Locate and identify every blood parasite.
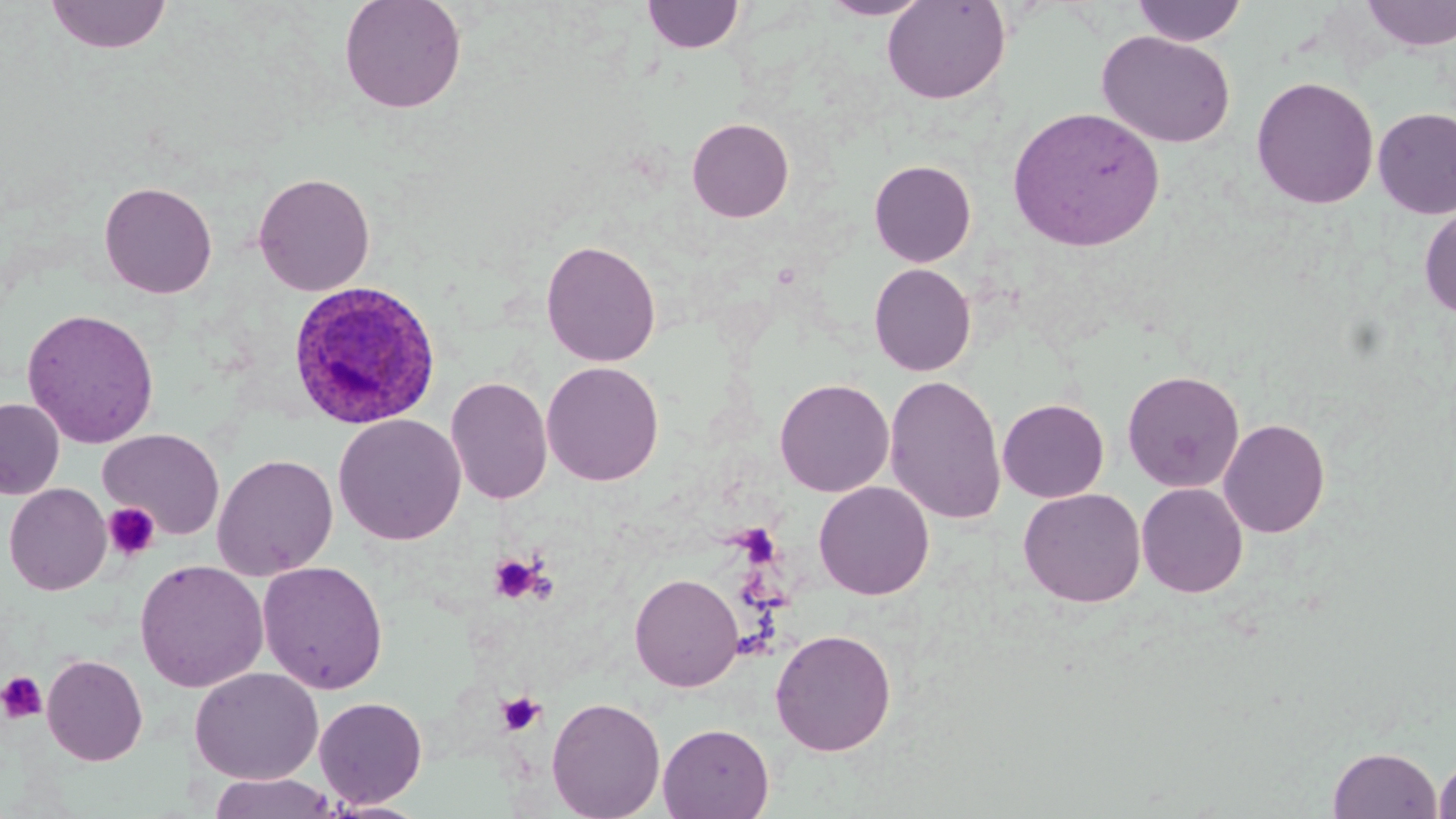
Approximate bounding boxes as (x1,y1)-(x2,y2) corner pairs in pixels.
Plasmodium ovale-infected red blood cells: (287,281)-(442,430).
No Plasmodium falciparum, Plasmodium malariae, Plasmodium vivax, Babesia divergens, or Trypanosoma brucei observed.

Platelet locations: (102,502)-(160,561), (488,552)-(545,604), (0,672)-(48,724), (497,690)-(545,736). Uninfected red blood cell locations: (45,0)-(172,55), (339,0)-(467,114), (818,0)-(934,20), (882,0)-(1010,104), (1360,0)-(1456,51), (641,1)-(745,54), (1131,1)-(1247,46), (1096,30)-(1236,148), (1250,76)-(1380,209), (1007,106)-(1165,252), (1373,107)-(1456,219), (686,117)-(794,222), (868,159)-(977,267), (253,172)-(375,297), (99,181)-(217,299), (1419,204)-(1456,320), (541,239)-(661,367), (869,263)-(977,376), (21,308)-(160,448), (541,361)-(664,486), (1122,369)-(1244,493), (884,375)-(1007,524), (445,376)-(553,505), (774,378)-(894,497), (0,398)-(65,500), (997,398)-(1109,503), (333,414)-(467,545), (1218,418)-(1331,538), (99,429)-(225,539), (212,453)-(338,580), (813,481)-(934,600), (1136,482)-(1249,598), (4,483)-(112,595), (1018,488)-(1146,608), (134,559)-(269,692), (257,561)-(389,694), (629,572)-(744,692), (770,627)-(897,756), (42,654)-(148,766), (189,666)-(324,784), (313,696)-(428,808), (546,696)-(666,819), (658,722)-(774,819), (1328,746)-(1443,818), (1433,751)-(1456,819), (207,772)-(339,818), (320,799)-(431,819). Slide-level diagnosis: Plasmodium ovale. One field of a larger specimen. Optical microscopy. May-Grünwald-Giemsa stain. 1000x magnification. Thin blood smear. Image is 1456×819 pixels.